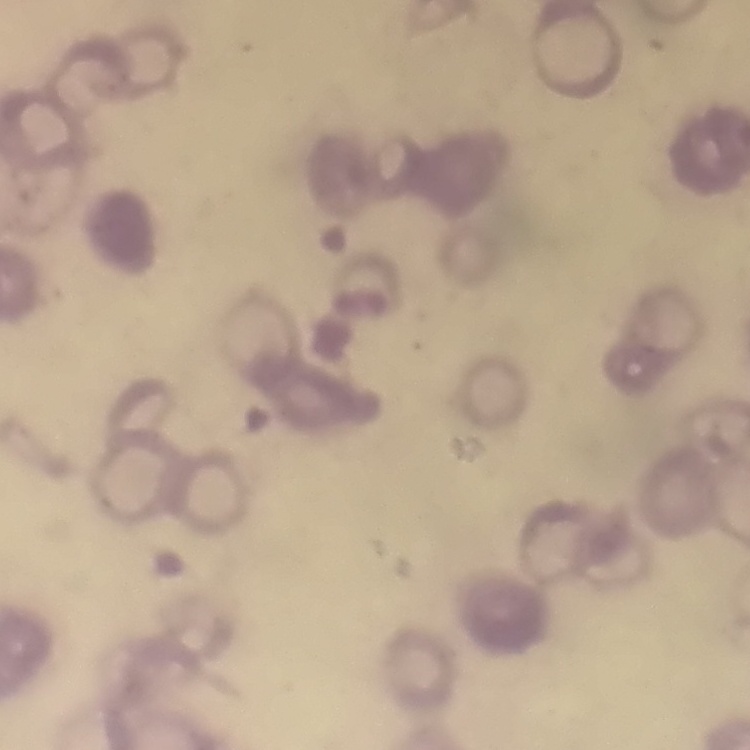
The erythrocytes show rouleaux formation. Square crop of a larger photomicrograph. Stained with either Field's or Giemsa. Thin blood film.